Classify this cell by malaria status.
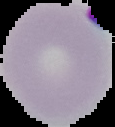

Parasitized.

Summary:
  - Image type: segmented cell region on a black background
  - Preparation: thin blood smear
  - Image size: 115×127 pixels